Locate every blood parasite and identify its species.
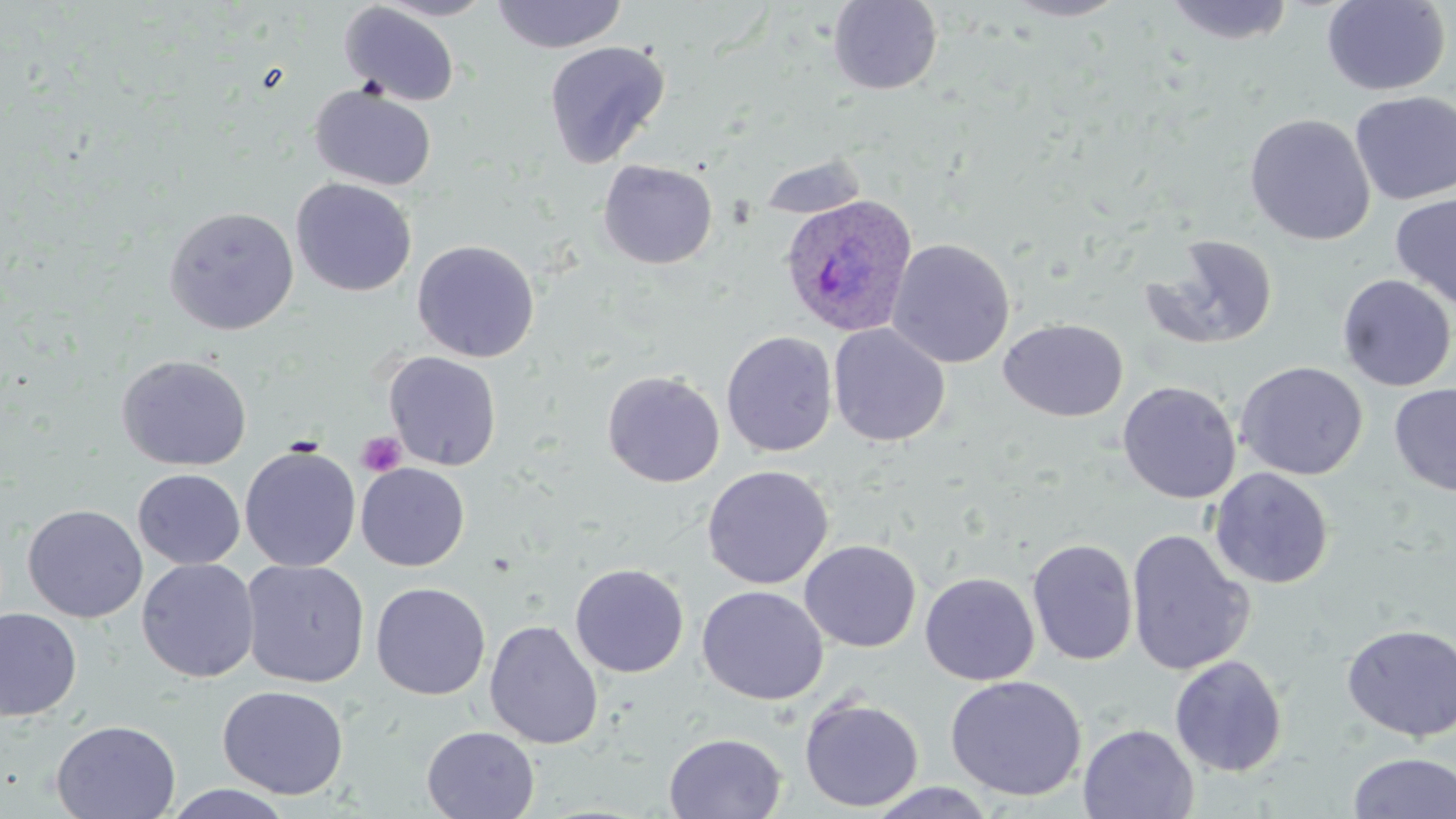
Approximate bounding boxes as named x1/y1/x2/y2 corners in pixels.
Plasmodium ovale-infected red blood cells: (x1=779, y1=193, x2=918, y2=337).
No Plasmodium falciparum, Plasmodium malariae, Plasmodium vivax, Babesia divergens, or Trypanosoma brucei observed.

Platelet locations: (x1=356, y1=431, x2=406, y2=477). Uninfected red blood cell locations: (x1=374, y1=0, x2=499, y2=21), (x1=490, y1=0, x2=628, y2=53), (x1=1001, y1=0, x2=1130, y2=22), (x1=1162, y1=0, x2=1296, y2=46), (x1=1321, y1=0, x2=1451, y2=96), (x1=828, y1=1, x2=943, y2=95), (x1=339, y1=2, x2=461, y2=107), (x1=543, y1=41, x2=670, y2=168), (x1=309, y1=83, x2=437, y2=191), (x1=1350, y1=91, x2=1456, y2=205), (x1=1244, y1=113, x2=1376, y2=246), (x1=757, y1=154, x2=870, y2=221), (x1=598, y1=160, x2=718, y2=270), (x1=291, y1=178, x2=417, y2=297), (x1=1390, y1=193, x2=1456, y2=310), (x1=163, y1=205, x2=300, y2=335), (x1=1139, y1=234, x2=1280, y2=352), (x1=887, y1=238, x2=1015, y2=368), (x1=412, y1=239, x2=540, y2=362), (x1=1336, y1=274, x2=1456, y2=391), (x1=999, y1=318, x2=1127, y2=422), (x1=828, y1=324, x2=950, y2=446), (x1=720, y1=331, x2=838, y2=457), (x1=383, y1=351, x2=502, y2=471), (x1=116, y1=354, x2=252, y2=471), (x1=1235, y1=361, x2=1368, y2=480), (x1=602, y1=370, x2=725, y2=487), (x1=1117, y1=381, x2=1241, y2=504), (x1=1389, y1=383, x2=1456, y2=498), (x1=240, y1=444, x2=361, y2=572), (x1=356, y1=462, x2=470, y2=571), (x1=701, y1=465, x2=834, y2=589), (x1=1209, y1=468, x2=1334, y2=589), (x1=133, y1=469, x2=245, y2=569), (x1=23, y1=504, x2=148, y2=623), (x1=1125, y1=528, x2=1256, y2=677), (x1=1026, y1=538, x2=1139, y2=666), (x1=799, y1=539, x2=921, y2=652), (x1=136, y1=558, x2=259, y2=683), (x1=240, y1=559, x2=370, y2=688), (x1=570, y1=563, x2=689, y2=678), (x1=920, y1=572, x2=1040, y2=685), (x1=371, y1=582, x2=491, y2=700), (x1=697, y1=585, x2=829, y2=705), (x1=0, y1=608, x2=82, y2=722), (x1=484, y1=619, x2=603, y2=749), (x1=1341, y1=623, x2=1456, y2=742), (x1=1169, y1=655, x2=1288, y2=777), (x1=945, y1=675, x2=1087, y2=801), (x1=217, y1=685, x2=349, y2=800), (x1=799, y1=696, x2=924, y2=812), (x1=51, y1=719, x2=181, y2=819), (x1=1078, y1=724, x2=1199, y2=819), (x1=421, y1=726, x2=540, y2=819), (x1=663, y1=732, x2=787, y2=818), (x1=1347, y1=751, x2=1456, y2=819), (x1=865, y1=782, x2=1000, y2=818), (x1=164, y1=784, x2=297, y2=819). Slide-level diagnosis: Plasmodium ovale. Image is 1456×819 pixels. May-Grünwald-Giemsa-stained preparation. Light microscopy. One field of a larger specimen. Thin blood smear. Captured at 1000x magnification.